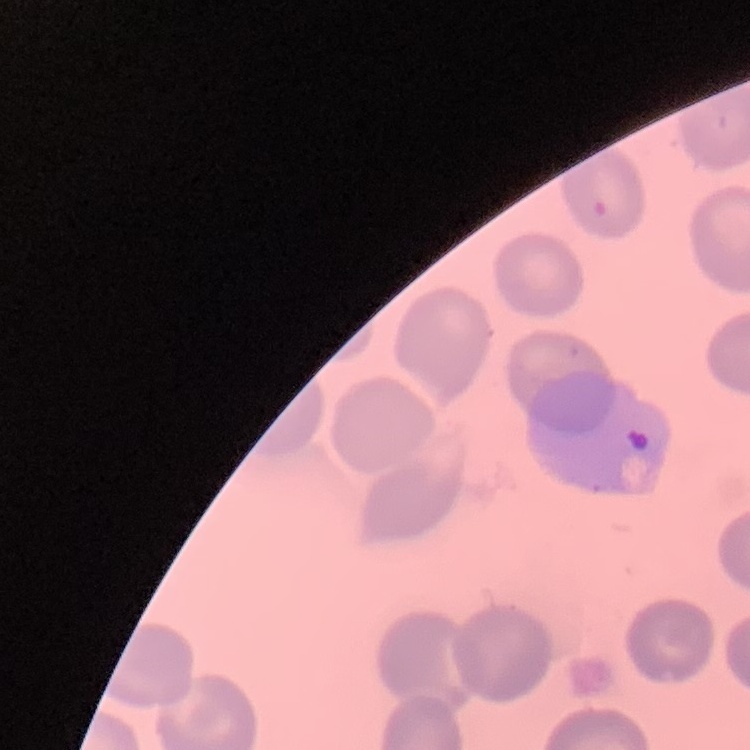 The red blood cells show no rouleaux formation. Thin blood smear. One tile cut from a larger photomicrograph. Stained with either Field's or Giemsa.